Identify the parasite.
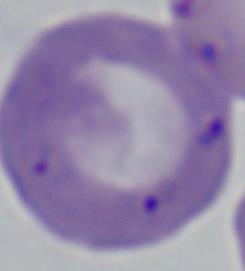

This is Babesia.

Micrograph. 1000x magnification.